Identify the parasite.
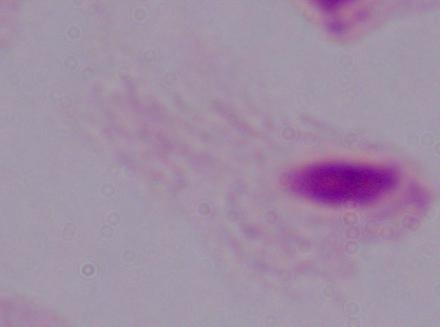

A trichomonad.

magnification = 1000x
modality = photomicrograph